Locate and identify every blood parasite.
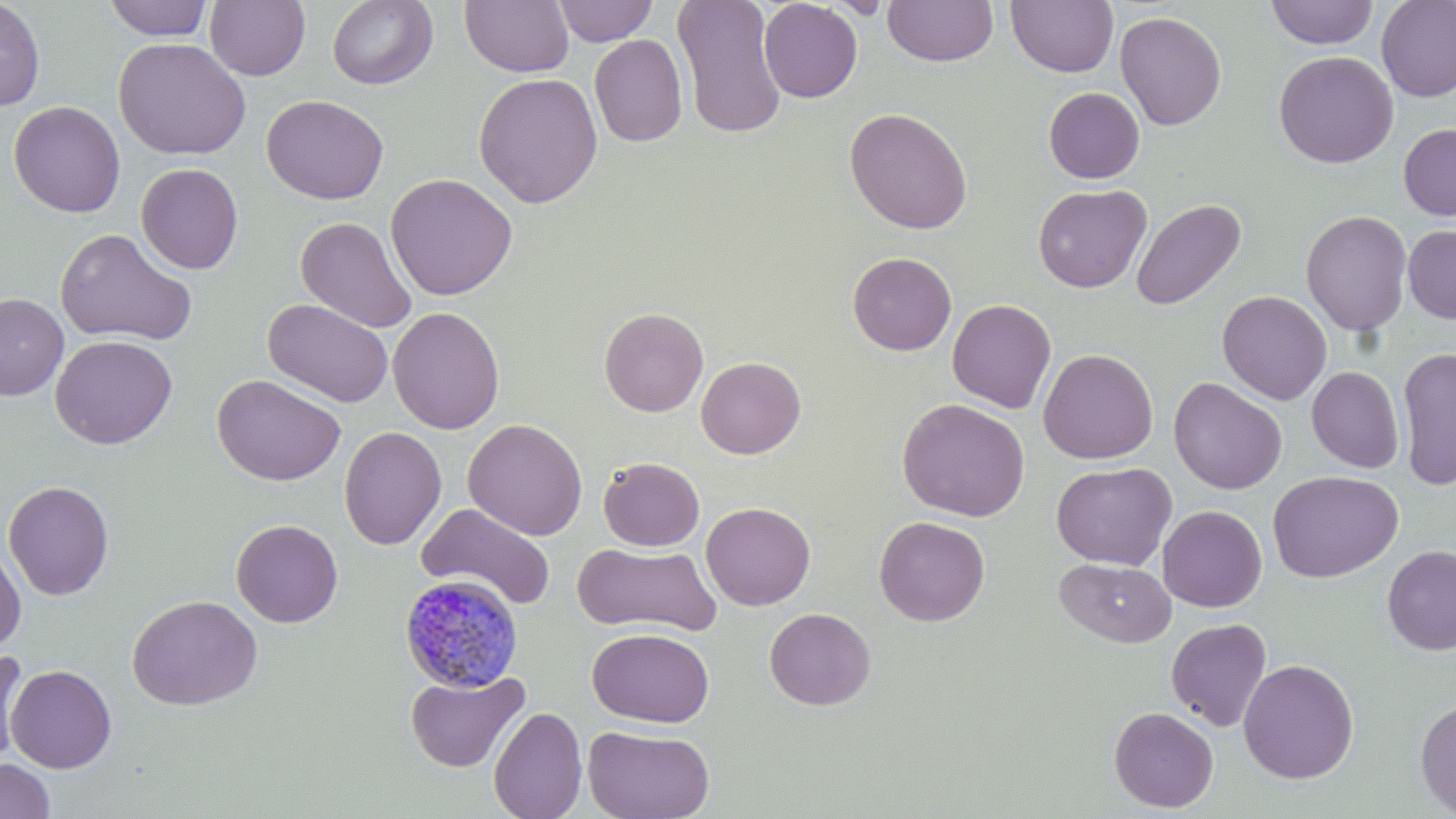
Approximate bounding boxes as (x1, y1, x2, y2) in pixels.
Plasmodium malariae-infected red blood cells: (398, 573, 524, 693).
No Plasmodium falciparum, Plasmodium ovale, Plasmodium vivax, Babesia divergens, or Trypanosoma brucei observed.

Uninfected red blood cell locations: (103, 0, 214, 41), (327, 0, 438, 90), (552, 0, 659, 46), (672, 0, 787, 139), (1375, 0, 1456, 102), (0, 1, 46, 112), (204, 1, 310, 81), (460, 1, 574, 77), (758, 1, 863, 103), (882, 1, 999, 67), (1006, 1, 1119, 78), (1264, 1, 1380, 49), (1114, 10, 1227, 130), (589, 34, 688, 148), (113, 37, 251, 160), (1273, 50, 1398, 169), (473, 72, 604, 208), (1043, 87, 1144, 183), (262, 94, 389, 205), (8, 101, 126, 218), (844, 107, 973, 234), (1398, 123, 1456, 221), (135, 162, 243, 274), (385, 172, 518, 301), (1032, 183, 1152, 293), (1130, 198, 1246, 312), (1300, 209, 1413, 336), (295, 216, 418, 334), (1403, 224, 1456, 324), (55, 227, 197, 347), (848, 252, 957, 356), (1217, 290, 1332, 405), (0, 293, 69, 400), (263, 298, 393, 408), (947, 298, 1057, 413), (388, 306, 505, 434), (599, 307, 708, 417), (50, 335, 177, 449), (1396, 346, 1456, 490), (1037, 348, 1159, 464), (696, 356, 806, 459), (1306, 366, 1405, 473), (212, 374, 346, 486), (1168, 377, 1288, 495), (896, 398, 1030, 521), (462, 418, 588, 540), (339, 426, 447, 549), (598, 457, 705, 551), (1050, 462, 1176, 570), (1267, 470, 1404, 583), (3, 480, 115, 600), (701, 502, 816, 610), (416, 503, 557, 611), (1157, 505, 1267, 612), (874, 515, 990, 627), (231, 519, 343, 628), (0, 542, 26, 652), (573, 542, 722, 636), (1382, 545, 1456, 656), (1055, 557, 1176, 647), (127, 594, 263, 711), (764, 608, 876, 711), (1165, 618, 1272, 732), (587, 627, 714, 727), (0, 648, 29, 768), (1238, 658, 1359, 784), (5, 664, 117, 773), (405, 669, 529, 773), (1414, 698, 1456, 817), (488, 706, 587, 819), (1109, 706, 1219, 813), (583, 725, 715, 819), (0, 758, 56, 819). Slide-level diagnosis: Plasmodium malariae. Thin blood smear. Single field of view. Light microscopy. Captured at 1000x magnification. Image is 1456×819 pixels. May-Grünwald-Giemsa-stained preparation.